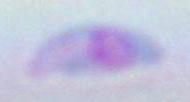
Summary:
  - Identification: Toxoplasma gondii
  - Magnification: 1000x
  - Modality: micrograph